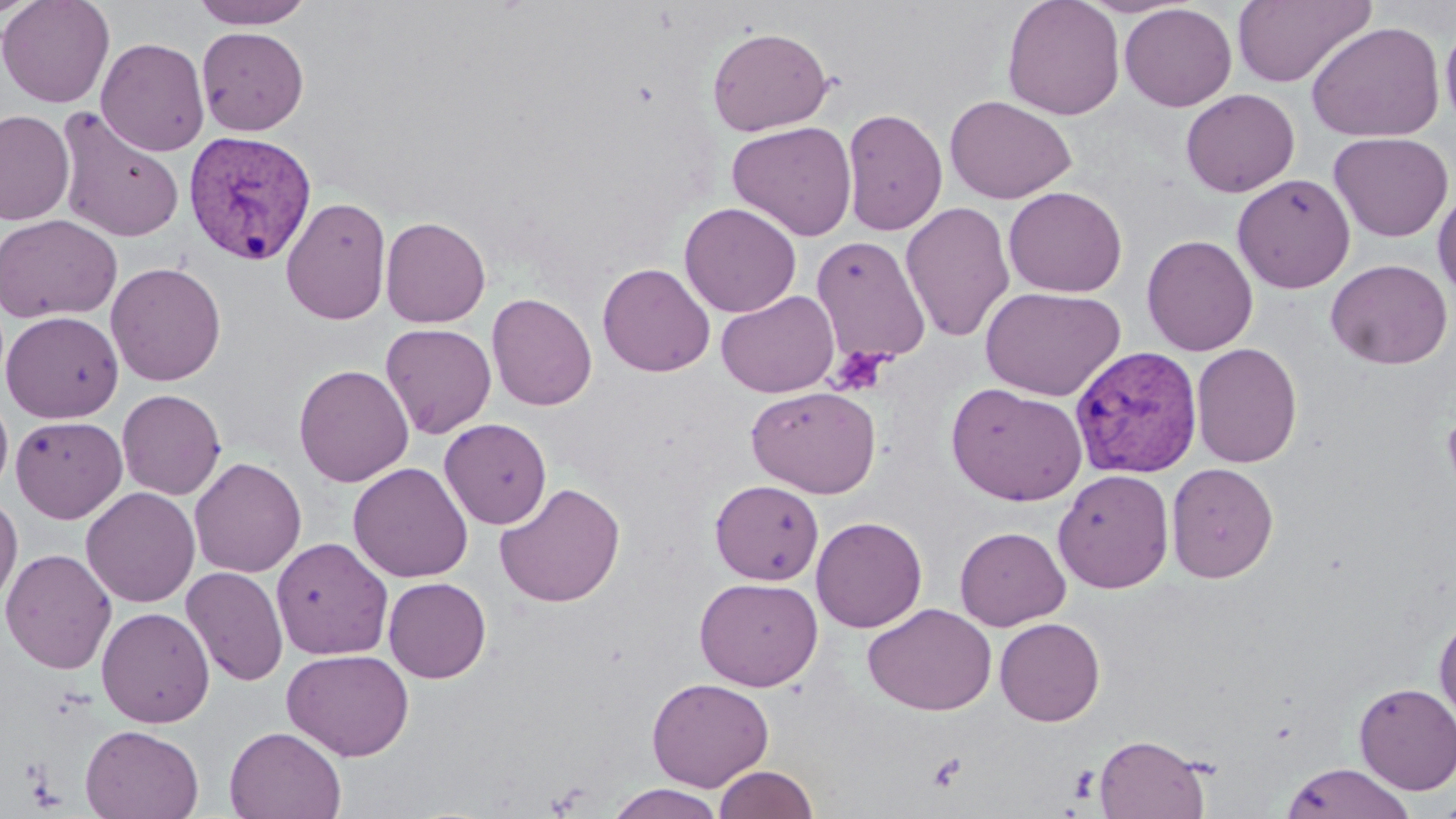
slide_level_diagnosis: Plasmodium vivax
stain: May-Grünwald-Giemsa
magnification: 1000x
modality: light microscopy
platelet_locations: 'approximate bounding boxes as (x1, y1, x2, y2) in pixels: (829, 346, 893, 397), (927, 753, 966, 792), (1068, 765, 1101, 804)'
image_size: 1456×819 pixels
plasmodium_vivax_infected_red_blood_cell_locations: 'approximate bounding boxes as (x1, y1, x2, y2) in pixels: (182, 130, 318, 266), (1070, 346, 1204, 479)'
field_of_view: one of a larger specimen
uninfected_red_blood_cell_locations: 'approximate bounding boxes as (x1, y1, x2, y2) in pixels: (0, 0, 44, 21), (0, 0, 115, 109), (191, 0, 314, 29), (1002, 0, 1125, 120), (1232, 0, 1376, 87), (1119, 3, 1237, 111), (1439, 11, 1456, 138), (1306, 22, 1445, 143), (196, 26, 309, 135), (707, 26, 834, 136), (96, 37, 210, 156), (1180, 88, 1300, 197), (944, 95, 1077, 203), (54, 107, 186, 243), (841, 107, 948, 236), (0, 109, 74, 225), (726, 121, 857, 241), (1328, 132, 1454, 242), (1232, 173, 1356, 293), (1003, 186, 1128, 297), (1433, 186, 1456, 304), (280, 195, 392, 325), (900, 201, 1015, 342), (679, 202, 801, 317), (0, 214, 122, 323), (380, 216, 491, 328), (1141, 234, 1258, 356), (810, 235, 931, 367), (1326, 258, 1452, 369), (105, 261, 227, 386), (597, 262, 715, 376), (979, 285, 1125, 401), (716, 290, 840, 398), (486, 292, 597, 411), (1, 311, 123, 423), (380, 322, 497, 439), (1191, 342, 1303, 468), (293, 364, 414, 488), (945, 382, 1087, 506), (746, 385, 881, 498), (117, 389, 226, 500), (0, 390, 14, 500), (10, 415, 127, 523), (439, 417, 552, 529), (189, 457, 306, 578), (348, 462, 473, 583), (1166, 462, 1279, 583), (1053, 468, 1174, 594), (709, 479, 824, 584), (494, 481, 626, 607), (81, 487, 200, 607), (0, 495, 22, 611), (811, 516, 928, 632), (955, 526, 1070, 630), (271, 537, 394, 660), (1, 548, 117, 674), (181, 566, 289, 686), (694, 576, 823, 691), (383, 577, 492, 683), (862, 602, 997, 716), (96, 606, 215, 728), (1434, 610, 1456, 730), (995, 617, 1106, 726), (281, 648, 414, 761), (646, 677, 774, 791), (1353, 682, 1456, 794), (80, 724, 203, 819), (224, 726, 347, 818), (1093, 733, 1211, 818), (1281, 762, 1415, 819), (713, 764, 819, 818), (606, 783, 726, 819), (1431, 795, 1456, 818)'
preparation: thin blood smear